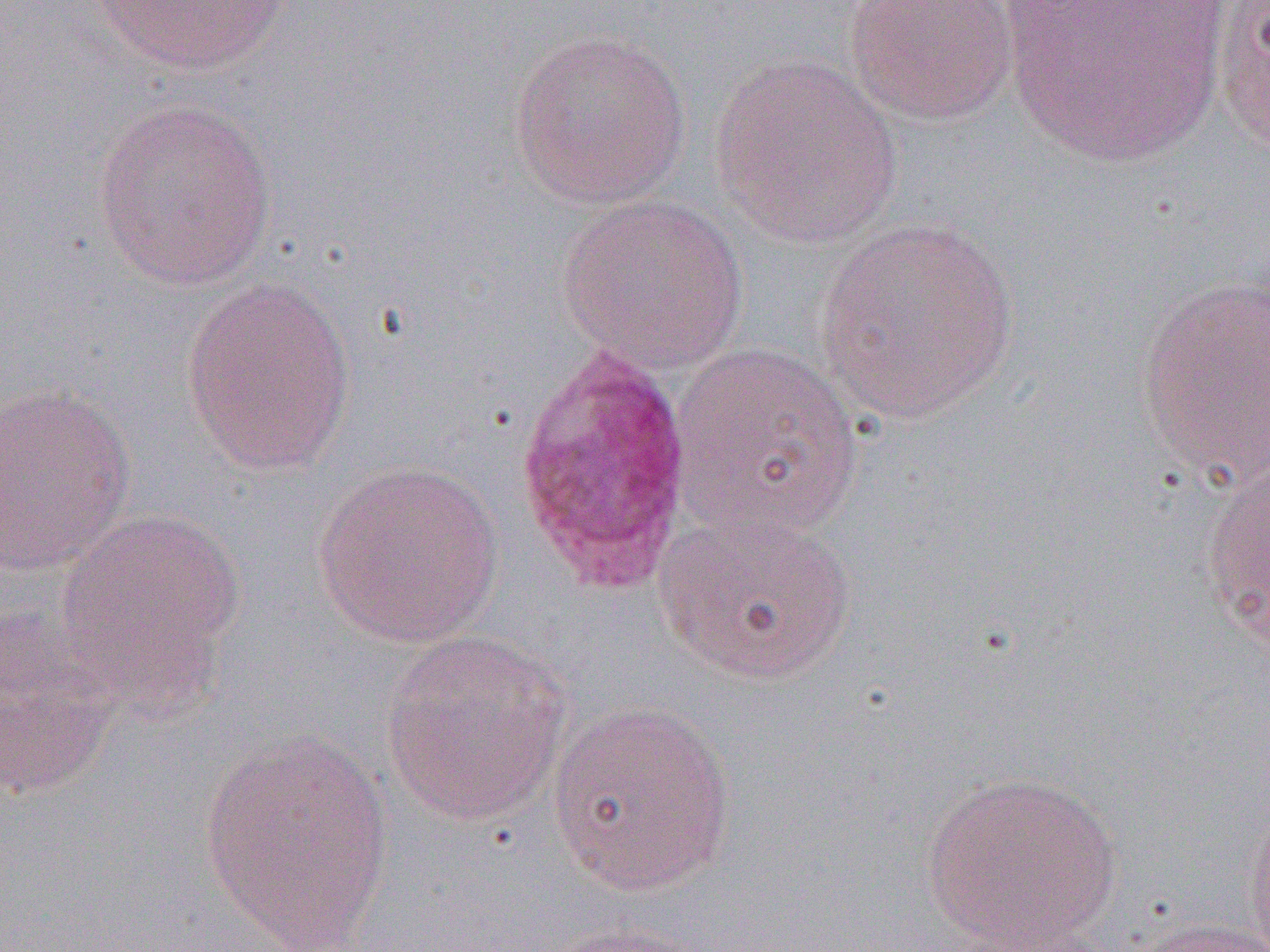
Summary:
  - Coordinate format: approximate bounding boxes as [x1, y1, x2, y2] in pixels
  - Uninfected red blood cell locations: [86, 0, 289, 77], [998, 0, 1231, 169], [1212, 0, 1270, 158], [843, 1, 1019, 126], [508, 28, 693, 209], [711, 55, 905, 249], [90, 99, 278, 293], [557, 193, 750, 374], [813, 216, 1020, 426], [1134, 273, 1269, 490], [180, 276, 357, 476], [668, 340, 865, 540], [0, 383, 137, 577], [312, 459, 505, 647], [1200, 467, 1270, 647], [653, 507, 858, 686], [53, 508, 245, 700], [0, 609, 122, 800], [379, 631, 572, 825], [546, 700, 738, 896], [199, 727, 395, 949], [921, 771, 1123, 949], [1242, 792, 1270, 952], [1122, 917, 1270, 952], [540, 921, 714, 951], [948, 921, 1129, 952]
  - Plasmodium ovale-infected red blood cell locations: [514, 342, 694, 599]
  - Slide-level diagnosis: Plasmodium ovale
  - Magnification: 1000x
  - Image size: 1270×952 pixels
  - Modality: optical microscopy
  - Field of view: one of a larger specimen
  - Preparation: thin blood film